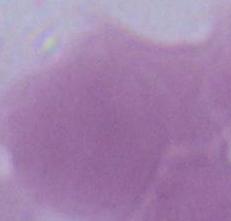
Summary:
  - Identification: erythrocyte
  - Modality: photomicrograph
  - Magnification: 1000x